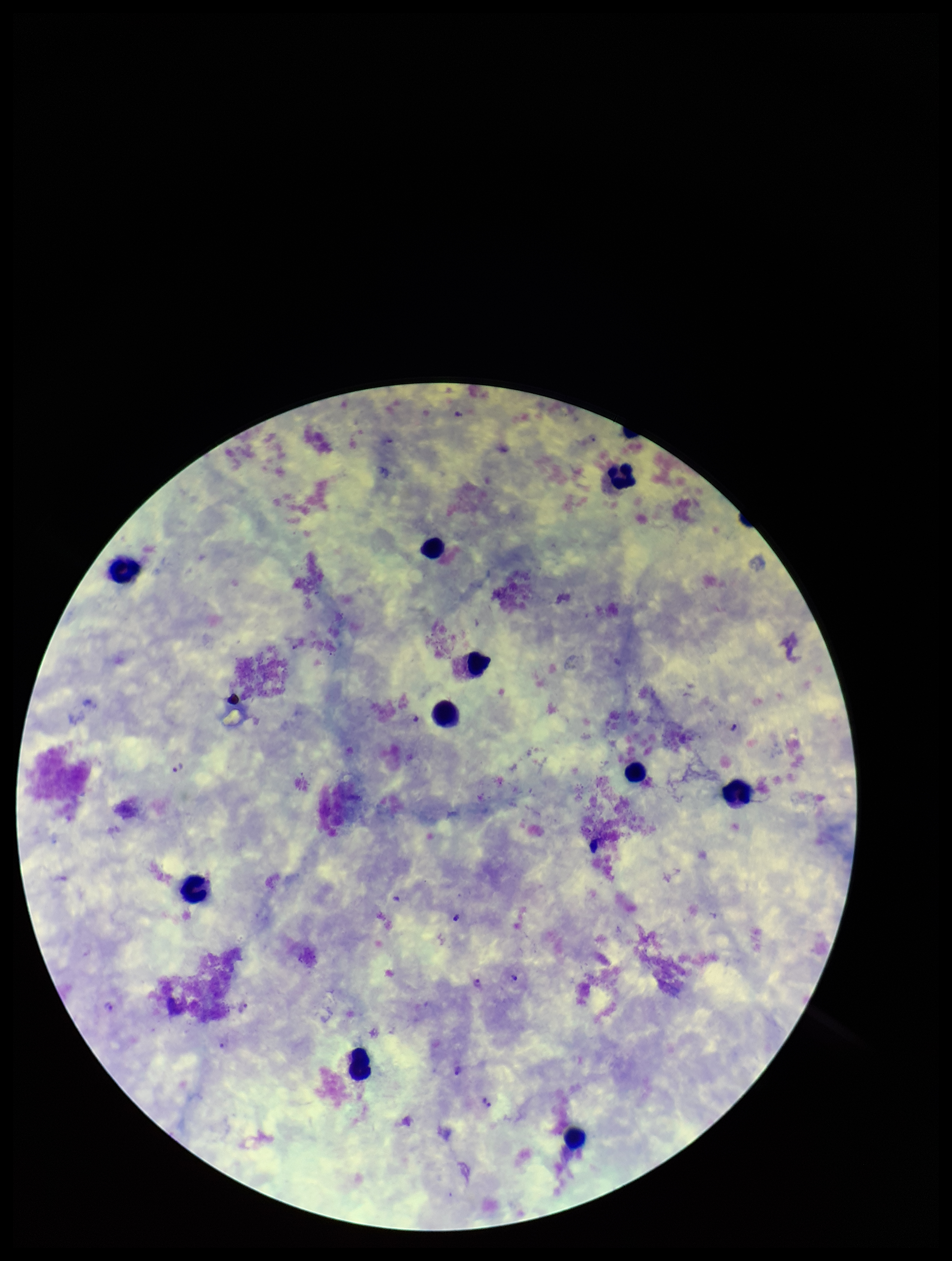
{
  "parasite_count": 7,
  "stain": "Giemsa",
  "species_reported_for_this_patient": "Plasmodium vivax",
  "preparation": "thick smear",
  "image_size": "952×1261 pixels",
  "field_of_view": "single",
  "leukocyte_count": 10,
  "plasmodium_parasites": "identified",
  "patient_malaria_status": "positive",
  "capture": "smartphone photograph through the microscope eyepiece"
}